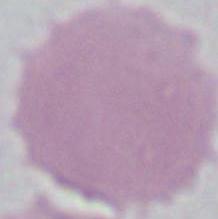
identification: erythrocyte
modality: photomicrograph
magnification: 1000x